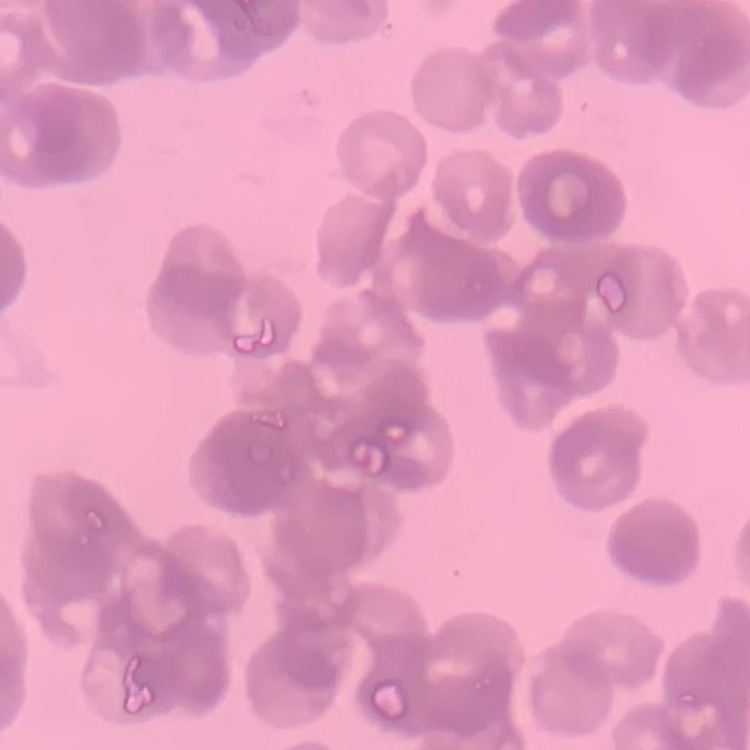
The red blood cells show rouleaux formation. Square crop of a larger photomicrograph. Thin blood smear. Stained with either Field's or Giemsa.